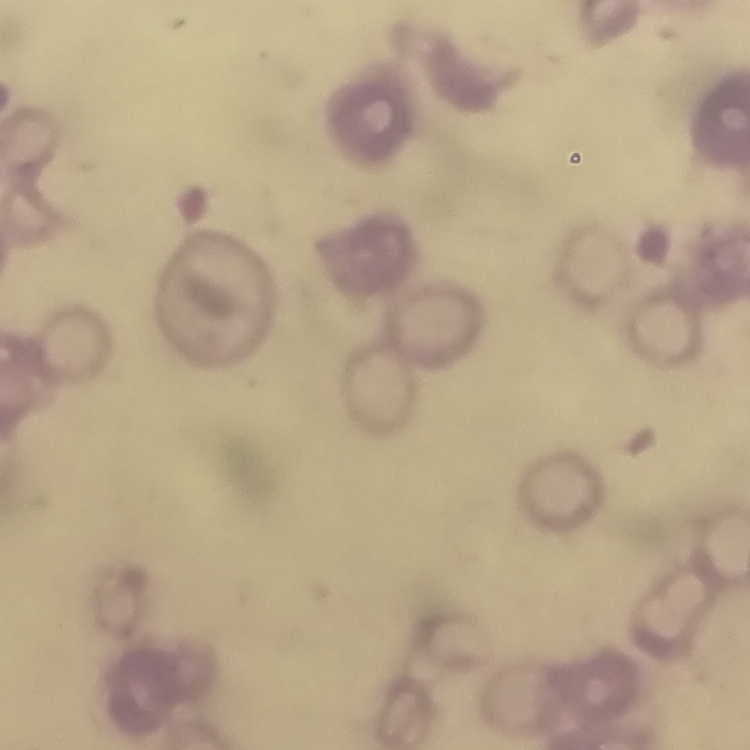 The erythrocytes show rouleaux formation. Thin blood smear. Square crop of a larger photomicrograph. Field's or Giemsa stain.